Name the parasite shown.
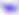
Toxoplasma gondii.

magnification: 400x
modality: photomicrograph